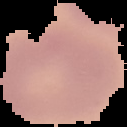

Summary:
  - Image type: segmented cell region on a black background
  - Preparation: thin blood smear
  - Image size: 127×127 pixels
  - Malaria status: uninfected